Outline each uninfected red blood cell.
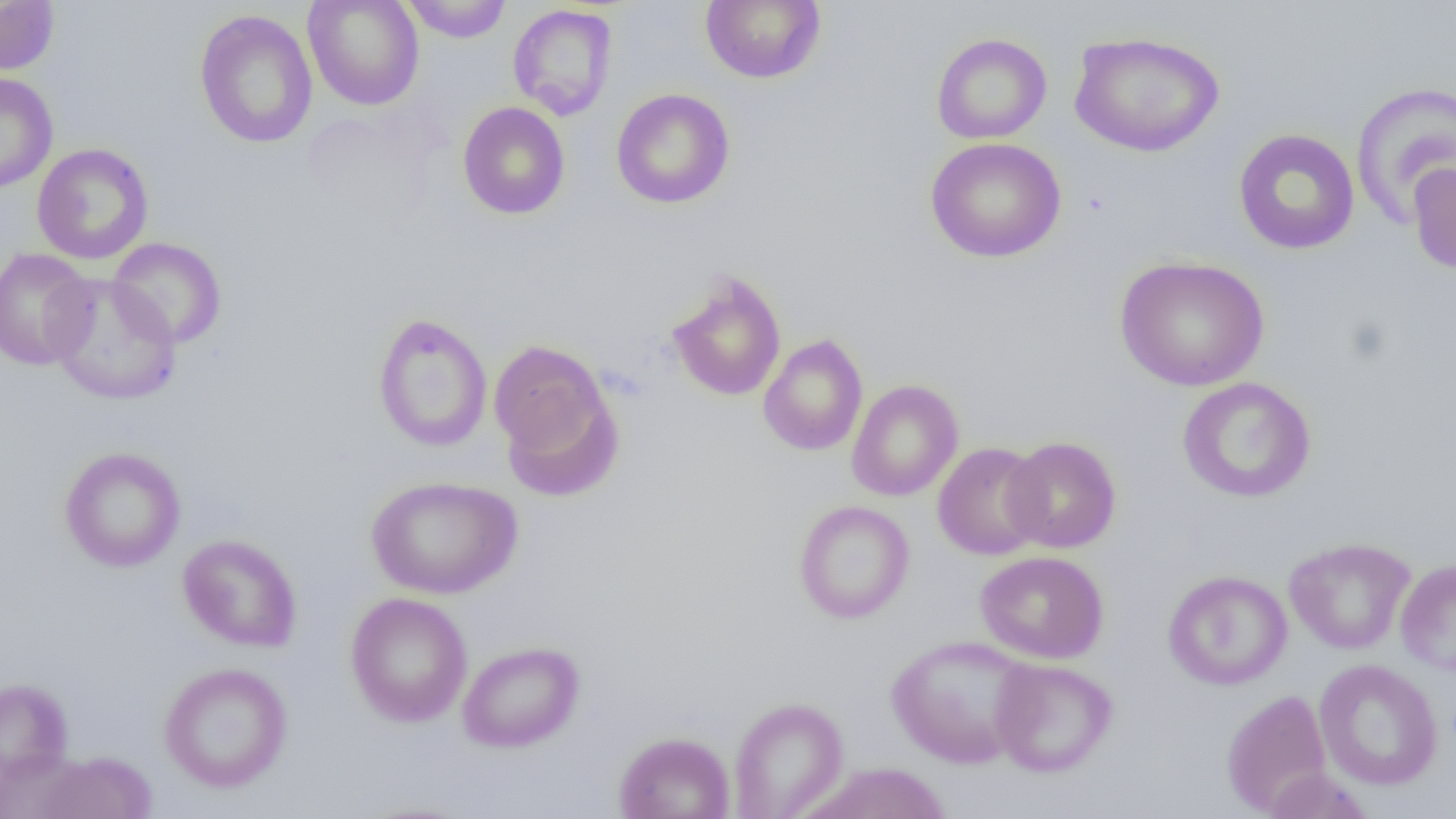

Approximate bounding boxes as (x1,y1)-(x2,y2) corner pairs in pixels.
Uninfected red blood cells: (303,0)-(424,111), (402,0)-(511,42), (700,0)-(826,84), (0,1)-(60,75), (507,4)-(618,121), (194,9)-(319,149), (1069,31)-(1225,157), (931,33)-(1052,144), (0,73)-(59,193), (1350,82)-(1456,228), (611,88)-(735,209), (457,102)-(570,220), (1232,128)-(1360,255), (924,137)-(1066,263), (31,142)-(154,265), (1407,161)-(1456,274), (108,237)-(227,349), (0,247)-(97,371), (1114,255)-(1269,391), (666,270)-(787,403), (46,272)-(183,406), (372,312)-(493,453), (757,334)-(868,457), (488,339)-(614,474), (1177,376)-(1316,503), (847,379)-(964,501), (1002,436)-(1122,553), (932,441)-(1048,560), (58,446)-(186,572), (366,475)-(523,600), (793,500)-(914,624), (175,531)-(298,791), (177,534)-(302,652), (1284,537)-(1416,655), (975,550)-(1109,663), (1395,558)-(1456,676), (1163,570)-(1292,690), (345,592)-(472,727), (885,635)-(1036,770), (457,640)-(585,753), (990,657)-(1118,777), (1313,659)-(1444,791), (158,662)-(293,793), (0,677)-(73,784), (1221,689)-(1333,815), (728,696)-(849,819), (614,730)-(735,819), (35,751)-(157,819), (804,763)-(953,819), (1262,767)-(1375,819).

Summary:
  - Slide-level diagnosis: negative for blood parasites
  - Preparation: thin blood film
  - Image size: 1456×819 pixels
  - Magnification: 1000x
  - Field of view: one of a larger specimen
  - Modality: optical microscopy